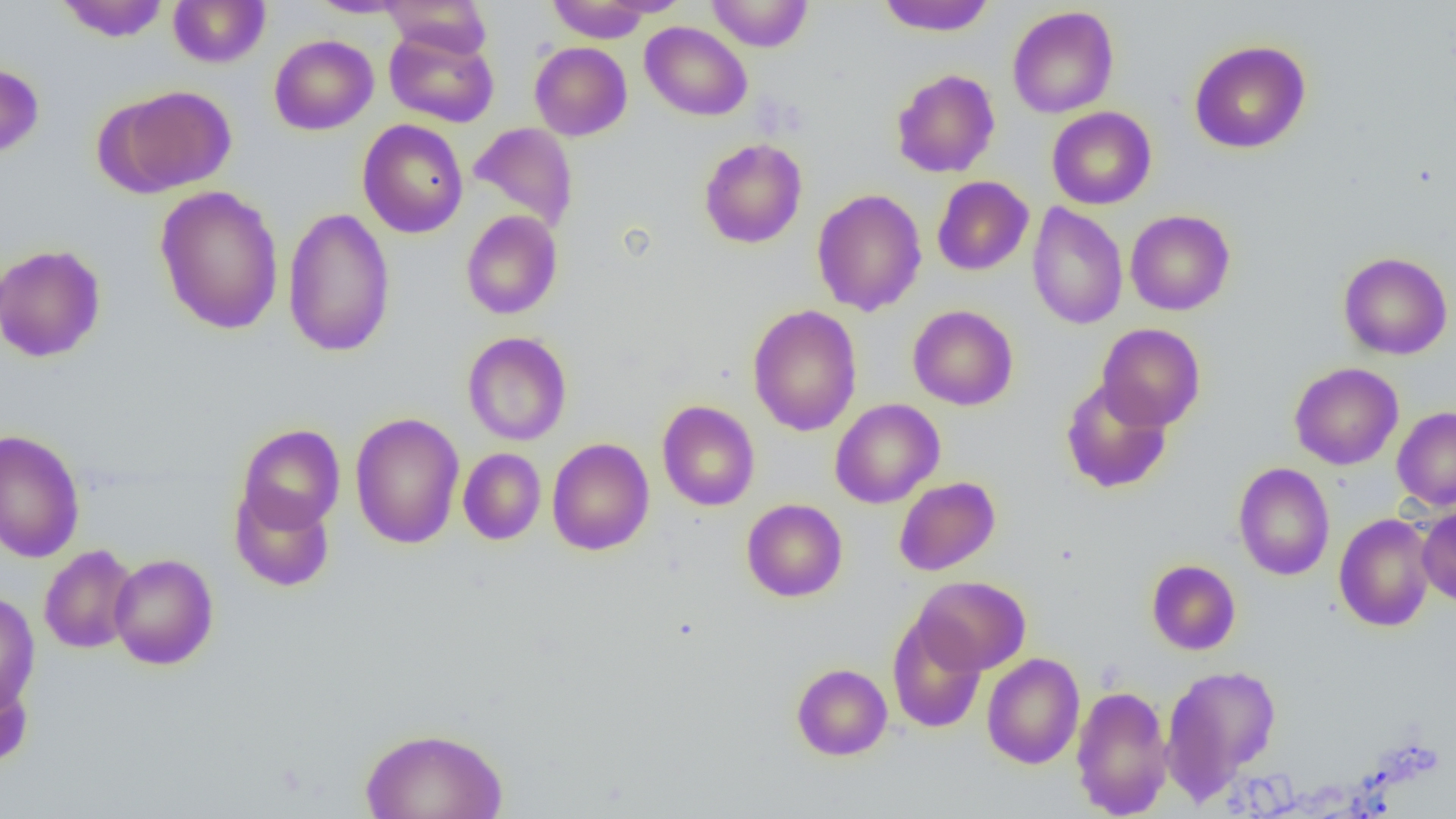
Summary:
  - Coordinate format: approximate bounding boxes as (x1,y1)-(x2,y2) corner pairs in pixels
  - Uninfected red blood cell locations: (56,0)-(169,42), (168,0)-(270,68), (308,0)-(412,18), (599,0)-(693,16), (706,0)-(813,52), (877,0)-(995,36), (382,1)-(492,57), (547,1)-(656,43), (1007,6)-(1119,119), (639,22)-(752,121), (384,28)-(499,128), (269,34)-(378,135), (1189,40)-(1311,154), (530,42)-(632,141), (0,61)-(44,159), (891,69)-(1000,178), (107,85)-(237,195), (1046,106)-(1157,209), (357,119)-(468,238), (469,122)-(579,232), (699,138)-(807,249), (931,176)-(1033,276), (154,185)-(284,335), (811,188)-(927,316), (1026,202)-(1128,330), (282,206)-(395,358), (461,210)-(563,320), (1125,210)-(1235,315), (0,243)-(106,363), (1338,252)-(1453,360), (748,304)-(862,436), (907,305)-(1018,411), (1096,323)-(1206,431), (462,332)-(572,446), (1289,362)-(1403,470), (1060,378)-(1173,494), (830,398)-(944,508), (657,400)-(760,511), (1392,406)-(1456,510), (350,412)-(465,549), (236,424)-(345,534), (0,429)-(85,563), (546,438)-(654,556), (458,447)-(546,545), (1233,463)-(1335,580), (893,476)-(1000,576), (230,486)-(335,592), (742,498)-(847,601), (1415,507)-(1456,606), (1334,513)-(1436,632), (39,544)-(139,654), (108,553)-(219,670), (1146,559)-(1241,655), (914,576)-(1031,675), (0,591)-(40,713), (887,612)-(987,733), (982,653)-(1085,769), (791,663)-(892,760), (1160,664)-(1281,801), (0,668)-(34,770), (1070,685)-(1173,818), (359,726)-(509,819)
  - Slide-level diagnosis: negative for blood parasites
  - Field of view: single
  - Modality: optical microscopy
  - Magnification: 1000x
  - Image size: 1456×819 pixels
  - Preparation: thin blood smear